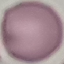

{
  "result": "negative for malaria parasites",
  "capture": "smartphone through the microscope eyepiece",
  "image_type": "cell patch, automatically extracted from a larger field of view and resized to 64 × 64 pixels",
  "stain": "Giemsa",
  "preparation": "thin blood smear"
}